Assess the morphology of the erythrocytes.
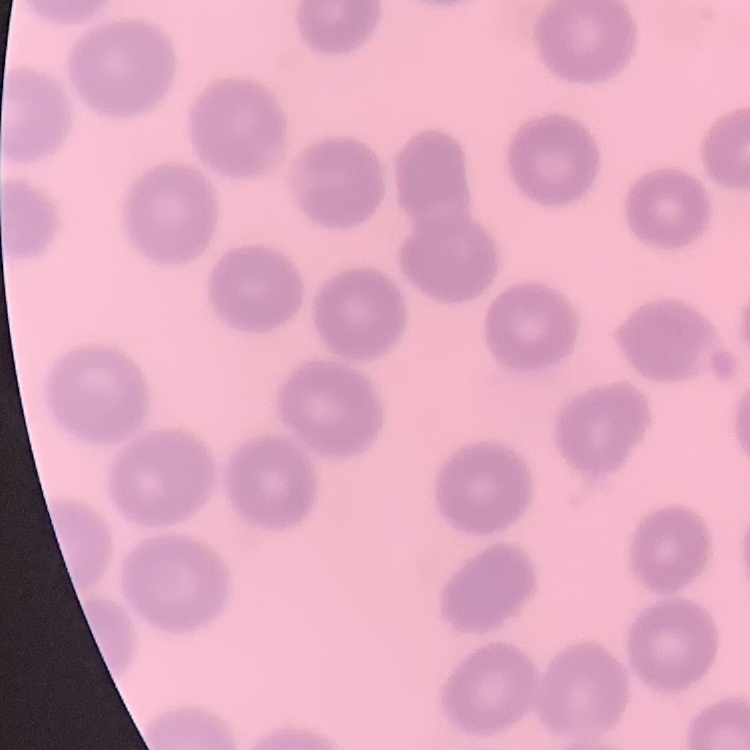
They show no rouleaux formation.

Summary:
  - Preparation: thin peripheral smear
  - Image type: square crop of a larger photomicrograph
  - Stain: Field's or Giemsa